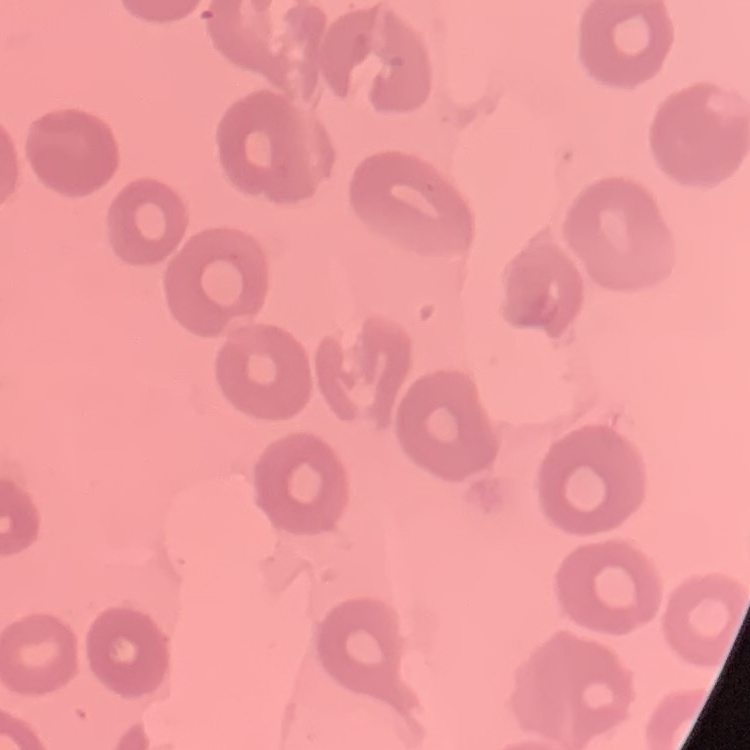
{
  "erythrocyte_morphology": "no rouleaux formation",
  "preparation": "thin blood smear",
  "stain": "Field's or Giemsa",
  "image_type": "one tile cut from a larger photomicrograph"
}